Locate every blood parasite and identify its species.
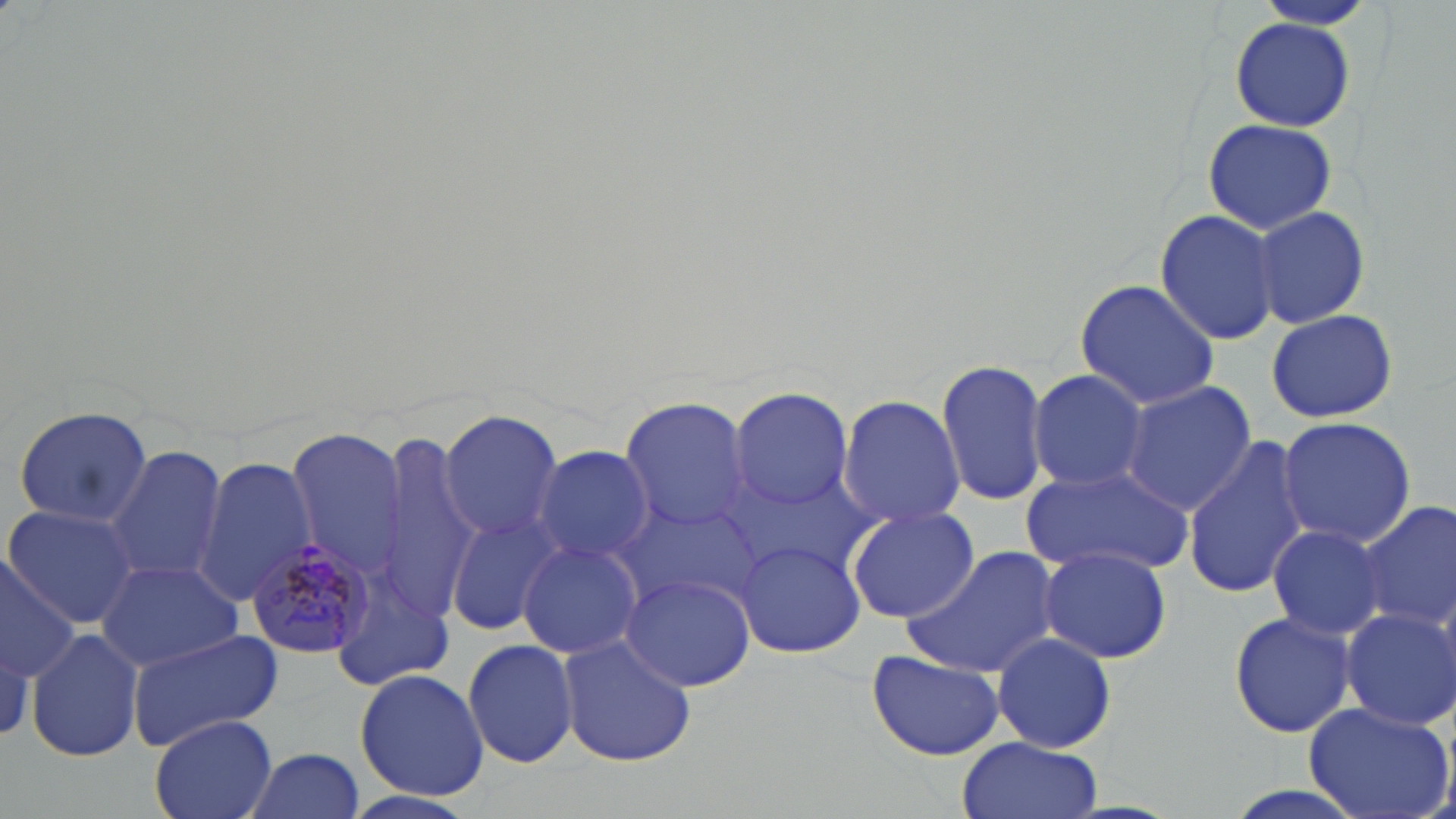

Approximate bounding boxes as [x1, y1, x2, y2] in pixels.
Plasmodium malariae-infected red blood cells: [246, 539, 377, 659].
No Plasmodium falciparum, Plasmodium ovale, Plasmodium vivax, Babesia divergens, or Trypanosoma brucei observed.

slide-level diagnosis = Plasmodium malariae
image size = 1456×819 pixels
modality = light microscopy
uninfected red blood cell locations = approximate bounding boxes as [x1, y1, x2, y2] in pixels: [1252, 1, 1376, 32], [1230, 17, 1355, 131], [1203, 116, 1336, 235], [1253, 206, 1369, 328], [1155, 207, 1283, 346], [1073, 278, 1221, 411], [1266, 308, 1397, 423], [935, 358, 1051, 507], [1028, 368, 1150, 493], [1120, 380, 1255, 515], [730, 387, 852, 512], [838, 393, 964, 531], [618, 396, 753, 535], [12, 405, 153, 529], [437, 409, 563, 541], [1277, 416, 1418, 550], [286, 427, 407, 580], [369, 436, 481, 622], [1183, 436, 1314, 597], [531, 444, 655, 567], [104, 445, 229, 583], [194, 458, 318, 605], [1023, 467, 1193, 575], [609, 491, 767, 622], [1355, 500, 1456, 633], [6, 505, 140, 627], [845, 505, 979, 625], [443, 512, 562, 637], [1265, 523, 1389, 640], [735, 539, 865, 659], [517, 540, 643, 658], [904, 545, 1063, 680], [1039, 545, 1173, 665], [0, 551, 81, 686], [96, 559, 246, 670], [332, 567, 457, 690], [620, 573, 755, 692], [1339, 607, 1455, 729], [1228, 609, 1358, 740], [26, 628, 144, 761], [127, 630, 284, 749], [556, 633, 699, 767], [990, 633, 1115, 753], [462, 637, 579, 767], [867, 649, 1005, 760], [355, 668, 488, 801], [1303, 701, 1454, 819], [149, 715, 278, 819], [956, 736, 1100, 819], [242, 747, 367, 819], [339, 789, 482, 819]
preparation = thin blood film
field of view = one of a larger specimen
stain = May-Grünwald-Giemsa
magnification = 1000x